Identify the parasite.
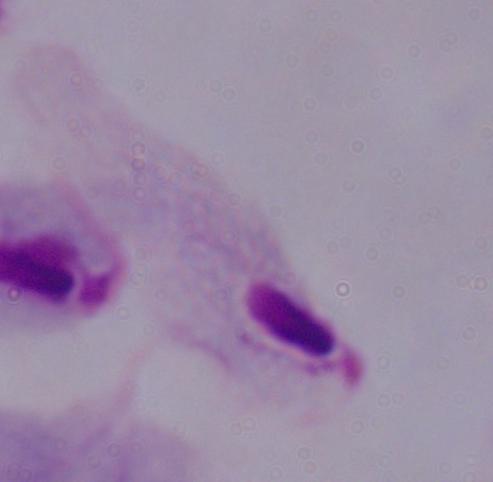
A trichomonad.

Captured at 1000x magnification. Micrograph.